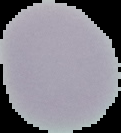
Summary:
  - Malaria status: uninfected
  - Image size: 121×133 pixels
  - Image type: segmented cell region with the area outside set to black
  - Preparation: thin blood film